Report the malaria status of this cell.
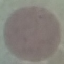

It is uninfected.

image type = cell patch, automatically extracted from a larger field of view and resized to 64 × 64 pixels
capture = smartphone camera at the microscope eyepiece
stain = Giemsa
preparation = thin blood film